Report the malaria status of this cell.
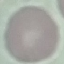

It is uninfected.

Thin smear of blood. Automatically extracted cell patch, resized to 64 × 64 pixels. Photographed with a smartphone camera at the microscope eyepiece. Giemsa-stained preparation.